Draw a bounding box around every leukocyte (white blood cell).
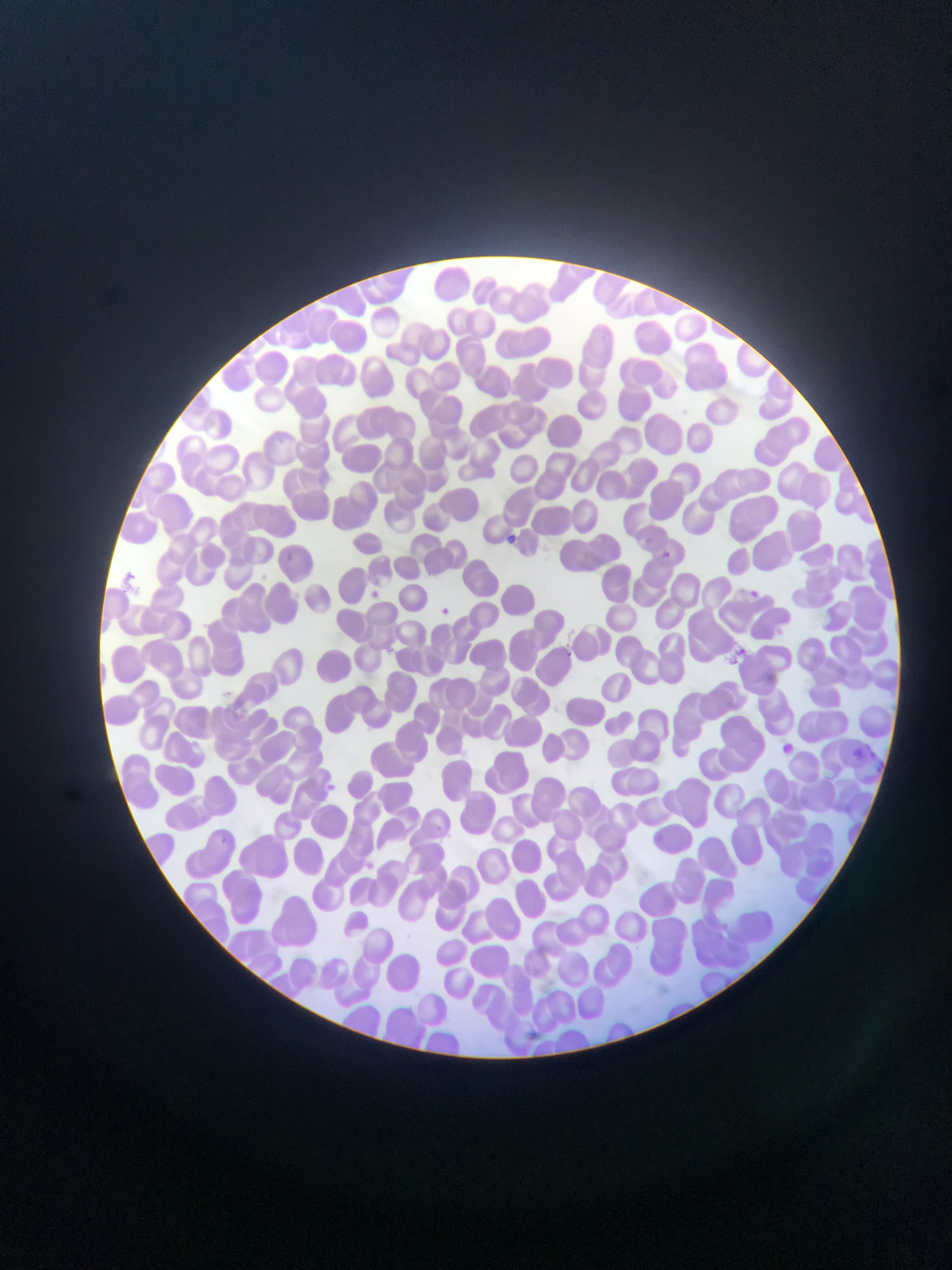

No leukocytes observed.

Approximate bounding boxes as [left, top, right, bottom] in pixels. Plasmodium parasite locations: [507, 532, 518, 543], [656, 549, 674, 565], [366, 587, 381, 601], [746, 588, 761, 602], [436, 604, 453, 619], [733, 645, 749, 662], [561, 648, 576, 662], [779, 742, 796, 757], [322, 781, 339, 796], [431, 824, 444, 836], [220, 835, 233, 849]. Thin blood smear. Image is 952×1270 pixels. Mobile-phone photograph taken through the microscope. Sample from Ghana. Single field of view.